Classify this cell by malaria status.
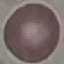

It is uninfected.

stain = Giemsa
capture = smartphone through the microscope eyepiece
preparation = thin blood film
image type = cell patch, automatically extracted from a larger field of view and resized to 64 × 64 pixels